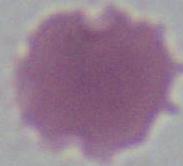
Summary:
  - Magnification: 1000x
  - Identification: erythrocyte
  - Modality: photomicrograph